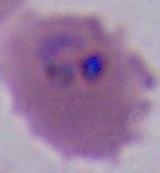
Summary:
  - Modality: photomicrograph
  - Identification: Plasmodium
  - Magnification: 400x or 1000x